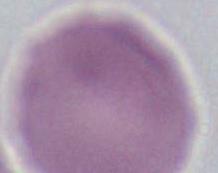 1000x magnification. Micrograph. A red blood cell is shown.